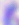
Summary:
  - Identification: Toxoplasma gondii
  - Modality: photomicrograph
  - Magnification: 400x